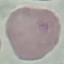
{
  "malaria_status": "uninfected",
  "preparation": "thin blood smear",
  "capture": "smartphone through the microscope eyepiece",
  "image_type": "cell patch, automatically extracted from a larger field of view and resized to 64 × 64 pixels",
  "stain": "Giemsa"
}